Point out each leukocyte.
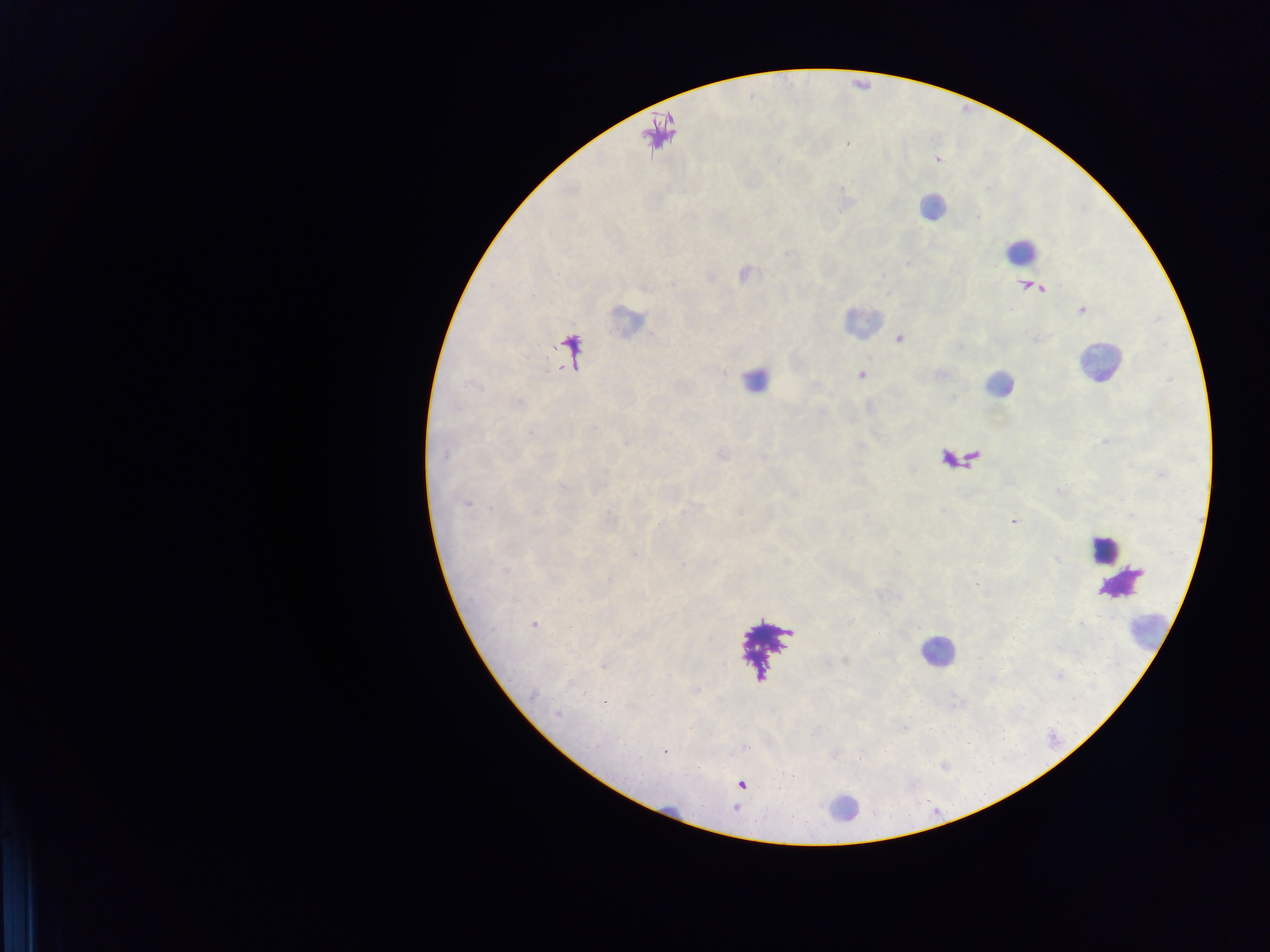

Approximate centers as [x, y] in pixels.
Leukocytes: [931, 208], [1020, 250], [625, 320], [865, 320], [1098, 363], [759, 379], [1001, 382], [1104, 549], [1141, 638], [936, 651], [844, 806].

Summary:
  - Malaria parasite locations: [860, 375], [530, 433], [1013, 522], [533, 626], [557, 715], [598, 746], [665, 752], [742, 785]
  - Preparation: thick blood smear
  - Capture: mobile-phone photograph through a microscope
  - Image size: 1270×952 pixels
  - Country: Ghana
  - Field of view: single